Locate platelets.
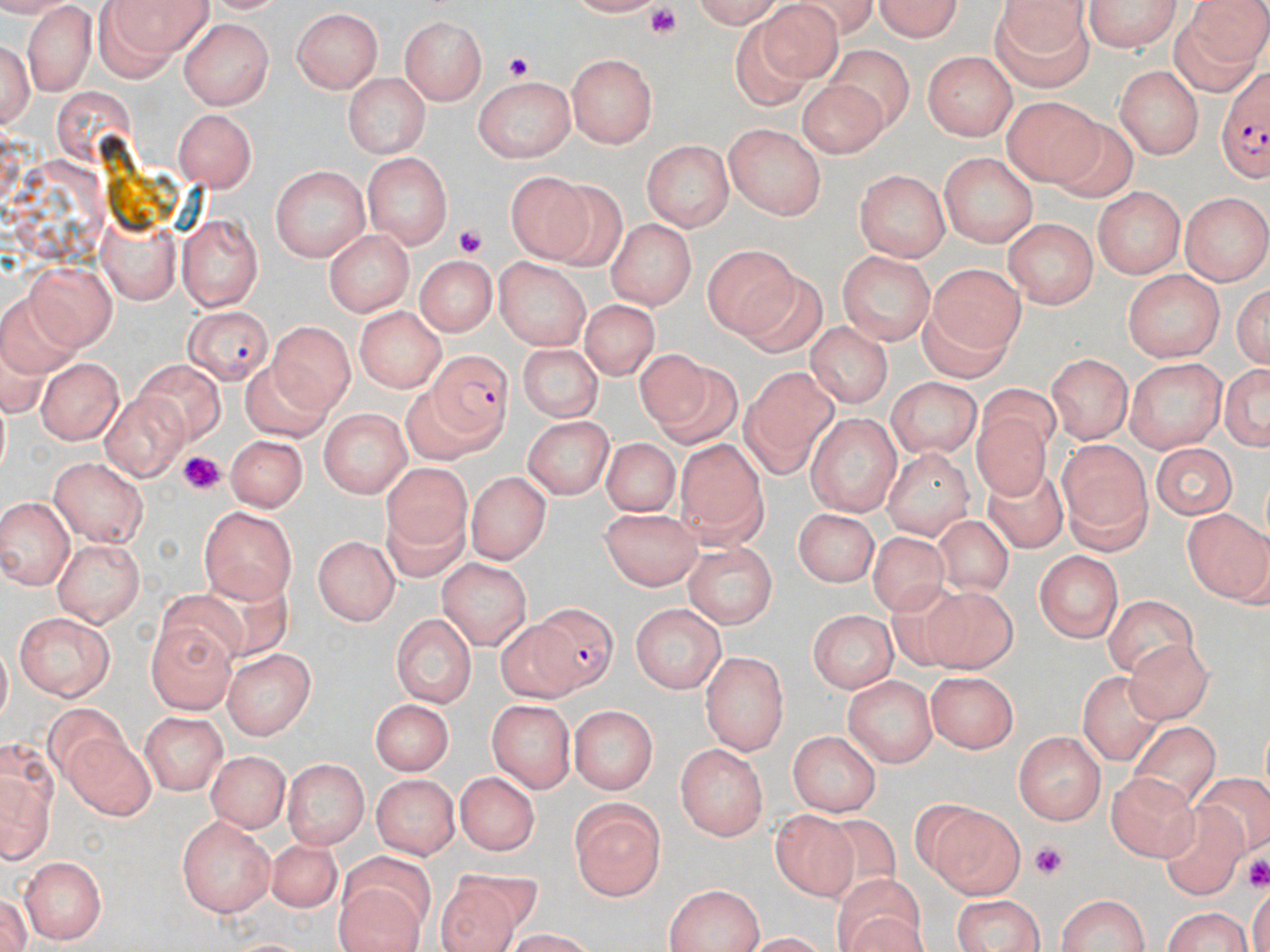

Approximate bounding boxes as named x1/y1/x2/y2 corners in pixels.
Platelets: (x1=638, y1=4, x2=687, y2=47), (x1=502, y1=52, x2=540, y2=88), (x1=454, y1=222, x2=490, y2=257), (x1=179, y1=452, x2=223, y2=491), (x1=1031, y1=838, x2=1065, y2=880), (x1=1249, y1=853, x2=1268, y2=888).

Plasmodium falciparum-infected red blood cell locations: (x1=1218, y1=63, x2=1268, y2=185), (x1=186, y1=303, x2=273, y2=385), (x1=427, y1=348, x2=517, y2=439), (x1=530, y1=603, x2=620, y2=694). Uninfected red blood cell locations: (x1=106, y1=0, x2=218, y2=62), (x1=684, y1=0, x2=784, y2=26), (x1=873, y1=0, x2=969, y2=42), (x1=1080, y1=0, x2=1183, y2=53), (x1=755, y1=1, x2=851, y2=82), (x1=984, y1=4, x2=1099, y2=90), (x1=23, y1=7, x2=93, y2=92), (x1=293, y1=7, x2=385, y2=93), (x1=1164, y1=14, x2=1262, y2=99), (x1=399, y1=15, x2=491, y2=105), (x1=727, y1=16, x2=813, y2=110), (x1=177, y1=21, x2=275, y2=108), (x1=0, y1=35, x2=37, y2=135), (x1=829, y1=43, x2=916, y2=131), (x1=925, y1=49, x2=1017, y2=138), (x1=566, y1=54, x2=655, y2=147), (x1=1115, y1=65, x2=1205, y2=160), (x1=339, y1=70, x2=432, y2=157), (x1=472, y1=73, x2=576, y2=163), (x1=799, y1=73, x2=889, y2=152), (x1=1003, y1=96, x2=1099, y2=188), (x1=173, y1=108, x2=258, y2=187), (x1=1042, y1=115, x2=1138, y2=204), (x1=723, y1=123, x2=829, y2=221), (x1=642, y1=138, x2=733, y2=232), (x1=362, y1=152, x2=453, y2=252), (x1=938, y1=152, x2=1039, y2=250), (x1=265, y1=165, x2=371, y2=263), (x1=508, y1=167, x2=599, y2=260), (x1=855, y1=171, x2=948, y2=263), (x1=557, y1=178, x2=631, y2=273), (x1=1092, y1=188, x2=1186, y2=282), (x1=1181, y1=192, x2=1267, y2=285), (x1=100, y1=215, x2=180, y2=304), (x1=177, y1=215, x2=265, y2=309), (x1=1001, y1=218, x2=1099, y2=310), (x1=609, y1=221, x2=693, y2=307), (x1=323, y1=228, x2=415, y2=314), (x1=702, y1=246, x2=800, y2=339), (x1=838, y1=249, x2=934, y2=345), (x1=416, y1=255, x2=495, y2=336), (x1=490, y1=258, x2=592, y2=348), (x1=925, y1=260, x2=1026, y2=352), (x1=30, y1=264, x2=124, y2=350), (x1=736, y1=269, x2=825, y2=357), (x1=1120, y1=269, x2=1229, y2=364), (x1=1235, y1=282, x2=1268, y2=369), (x1=574, y1=300, x2=663, y2=383), (x1=355, y1=305, x2=448, y2=389), (x1=271, y1=318, x2=359, y2=413), (x1=807, y1=323, x2=890, y2=407), (x1=516, y1=342, x2=601, y2=420), (x1=633, y1=348, x2=713, y2=429), (x1=1045, y1=353, x2=1134, y2=444), (x1=1126, y1=355, x2=1229, y2=452), (x1=37, y1=357, x2=126, y2=442), (x1=136, y1=357, x2=224, y2=444), (x1=1219, y1=357, x2=1269, y2=459), (x1=248, y1=360, x2=333, y2=447), (x1=751, y1=363, x2=835, y2=460), (x1=887, y1=377, x2=981, y2=460), (x1=396, y1=381, x2=477, y2=464), (x1=102, y1=391, x2=186, y2=479), (x1=322, y1=410, x2=409, y2=498), (x1=808, y1=410, x2=905, y2=513), (x1=974, y1=410, x2=1053, y2=506), (x1=524, y1=415, x2=614, y2=501), (x1=227, y1=431, x2=308, y2=509), (x1=676, y1=437, x2=761, y2=527), (x1=600, y1=438, x2=682, y2=517), (x1=1057, y1=438, x2=1149, y2=551), (x1=1151, y1=440, x2=1237, y2=519), (x1=882, y1=448, x2=974, y2=537), (x1=47, y1=456, x2=148, y2=545), (x1=381, y1=463, x2=473, y2=577), (x1=981, y1=464, x2=1072, y2=552), (x1=467, y1=470, x2=548, y2=565), (x1=0, y1=497, x2=74, y2=590), (x1=199, y1=506, x2=296, y2=601), (x1=796, y1=507, x2=878, y2=590), (x1=602, y1=509, x2=702, y2=587), (x1=1183, y1=509, x2=1269, y2=605), (x1=929, y1=514, x2=1021, y2=598), (x1=869, y1=529, x2=949, y2=619), (x1=312, y1=533, x2=398, y2=626), (x1=52, y1=539, x2=145, y2=623), (x1=680, y1=541, x2=781, y2=631), (x1=1033, y1=549, x2=1125, y2=643), (x1=436, y1=558, x2=530, y2=649), (x1=158, y1=586, x2=250, y2=666), (x1=921, y1=588, x2=1017, y2=667), (x1=1102, y1=593, x2=1201, y2=678), (x1=631, y1=603, x2=726, y2=693), (x1=805, y1=607, x2=900, y2=691), (x1=15, y1=610, x2=118, y2=701), (x1=391, y1=611, x2=477, y2=708), (x1=496, y1=618, x2=577, y2=703), (x1=145, y1=624, x2=236, y2=711), (x1=1123, y1=639, x2=1216, y2=727), (x1=225, y1=646, x2=317, y2=738), (x1=704, y1=652, x2=787, y2=754), (x1=928, y1=669, x2=1020, y2=756), (x1=1072, y1=672, x2=1166, y2=763), (x1=844, y1=673, x2=936, y2=766), (x1=369, y1=697, x2=453, y2=773), (x1=487, y1=698, x2=577, y2=790), (x1=43, y1=700, x2=126, y2=781), (x1=569, y1=703, x2=655, y2=794), (x1=139, y1=712, x2=226, y2=794), (x1=1121, y1=721, x2=1224, y2=811), (x1=790, y1=729, x2=881, y2=818), (x1=1015, y1=730, x2=1106, y2=825), (x1=64, y1=732, x2=155, y2=821), (x1=676, y1=743, x2=771, y2=839), (x1=207, y1=750, x2=289, y2=834), (x1=283, y1=757, x2=368, y2=851), (x1=2, y1=766, x2=52, y2=867), (x1=370, y1=772, x2=458, y2=859), (x1=1197, y1=772, x2=1270, y2=848), (x1=453, y1=773, x2=541, y2=856), (x1=1104, y1=774, x2=1202, y2=867), (x1=569, y1=796, x2=668, y2=900), (x1=1162, y1=798, x2=1251, y2=895), (x1=927, y1=801, x2=1025, y2=897), (x1=771, y1=809, x2=861, y2=905), (x1=809, y1=814, x2=904, y2=910), (x1=175, y1=815, x2=275, y2=921), (x1=266, y1=840, x2=342, y2=909), (x1=335, y1=850, x2=434, y2=921), (x1=19, y1=855, x2=104, y2=944), (x1=439, y1=872, x2=546, y2=952), (x1=834, y1=872, x2=921, y2=952), (x1=332, y1=882, x2=428, y2=952), (x1=665, y1=884, x2=764, y2=952), (x1=1053, y1=891, x2=1154, y2=952), (x1=949, y1=894, x2=1051, y2=952), (x1=1159, y1=905, x2=1257, y2=952). Slide-level diagnosis: Plasmodium falciparum. Optical microscopy. Single field of view. Captured at 1000x magnification. Image is 1270×952 pixels. Thin blood film. May-Grünwald-Giemsa-stained preparation.